State which cell type is depicted.
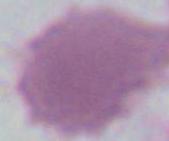
An erythrocyte.

magnification = 1000x
modality = micrograph